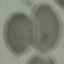
Summary:
  - Result: no malaria parasites seen
  - Image type: cell patch, automatically extracted from a larger field of view and resized to 64 × 64 pixels
  - Stain: Giemsa
  - Preparation: thin blood smear
  - Capture: smartphone camera at the microscope eyepiece